Look for parasitized red blood cells.
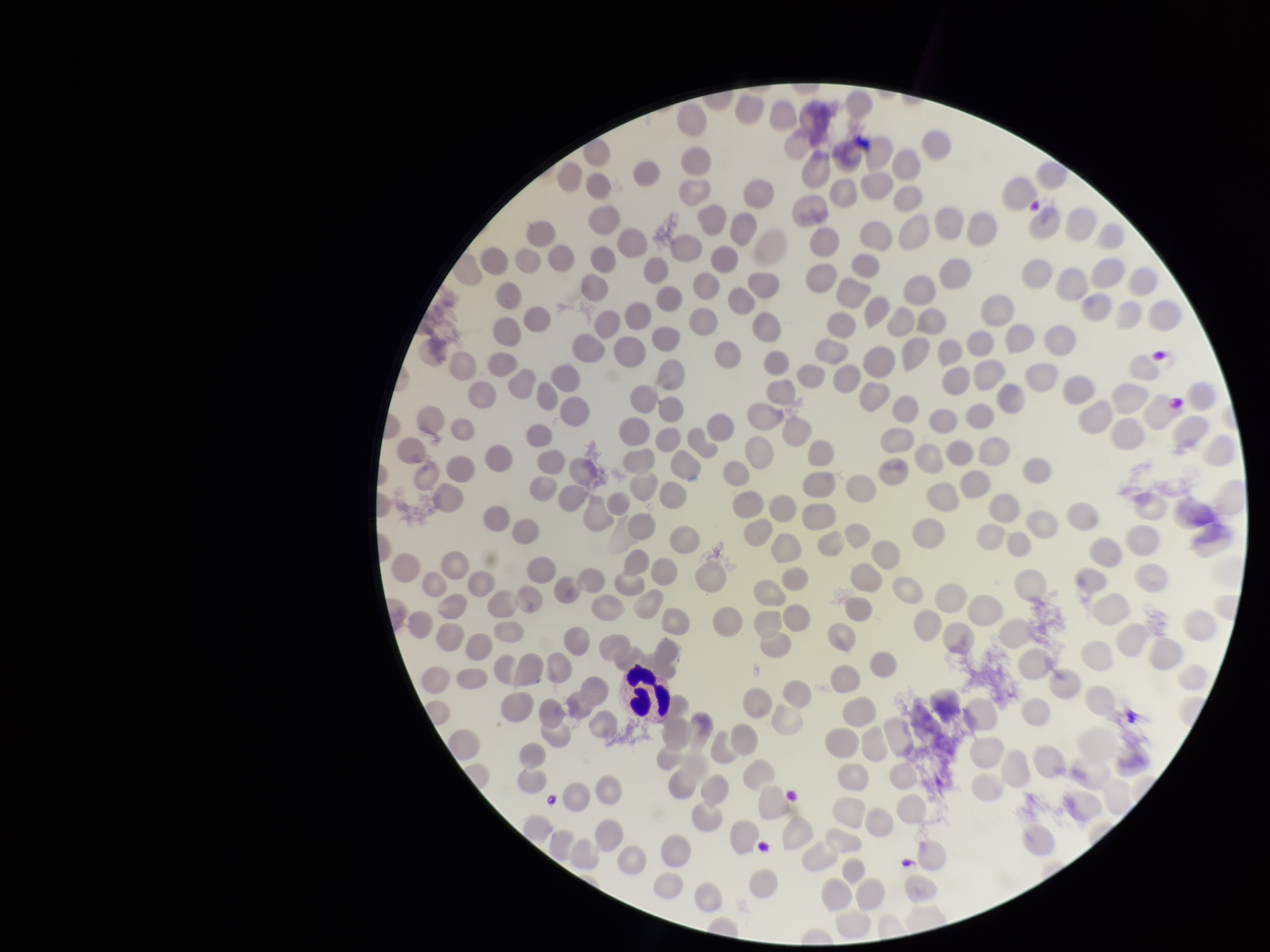
None detected.

Single field of view. Image is 1270×952 pixels. Patient malaria status: negative. Photographed through the microscope eyepiece with a smartphone camera. Parasitized red blood cell count: 0. Preparation: thin smear. Stained with Giemsa. Red blood cell count: 233.